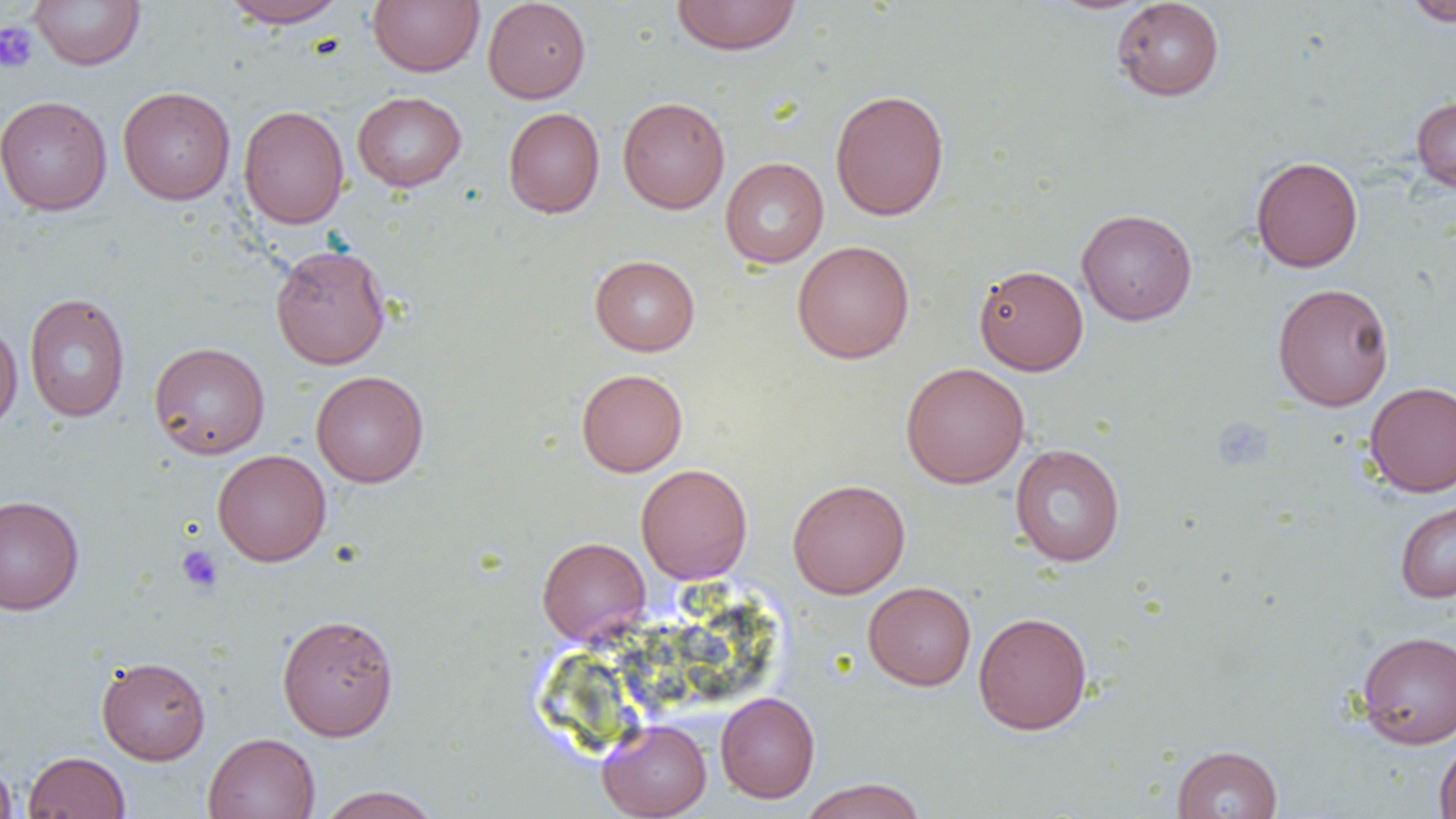

slide-level diagnosis = no evidence of blood parasites
uninfected red blood cell locations = approximate bounding boxes as named x1/y1/x2/y2 corners in pixels: (x1=29, y1=0, x2=145, y2=70), (x1=219, y1=0, x2=350, y2=28), (x1=367, y1=0, x2=484, y2=76), (x1=482, y1=0, x2=591, y2=103), (x1=670, y1=0, x2=801, y2=55), (x1=1112, y1=0, x2=1225, y2=101), (x1=1404, y1=0, x2=1456, y2=25), (x1=118, y1=86, x2=235, y2=205), (x1=830, y1=88, x2=950, y2=221), (x1=352, y1=91, x2=466, y2=192), (x1=0, y1=95, x2=112, y2=216), (x1=618, y1=96, x2=730, y2=213), (x1=1411, y1=97, x2=1456, y2=194), (x1=238, y1=105, x2=349, y2=229), (x1=503, y1=107, x2=604, y2=218), (x1=1251, y1=156, x2=1363, y2=272), (x1=720, y1=157, x2=829, y2=268), (x1=1076, y1=208, x2=1197, y2=325), (x1=792, y1=240, x2=914, y2=363), (x1=271, y1=243, x2=391, y2=369), (x1=589, y1=254, x2=700, y2=356), (x1=974, y1=264, x2=1088, y2=375), (x1=1272, y1=282, x2=1394, y2=412), (x1=24, y1=293, x2=130, y2=422), (x1=0, y1=317, x2=23, y2=434), (x1=148, y1=341, x2=270, y2=459), (x1=901, y1=362, x2=1030, y2=489), (x1=576, y1=368, x2=688, y2=476), (x1=310, y1=370, x2=429, y2=487), (x1=1364, y1=381, x2=1456, y2=497), (x1=1009, y1=444, x2=1125, y2=567), (x1=212, y1=449, x2=331, y2=567), (x1=636, y1=463, x2=753, y2=584), (x1=787, y1=478, x2=910, y2=598), (x1=0, y1=495, x2=84, y2=615), (x1=1395, y1=499, x2=1456, y2=603), (x1=536, y1=536, x2=651, y2=646), (x1=863, y1=582, x2=976, y2=690), (x1=973, y1=611, x2=1092, y2=735), (x1=276, y1=613, x2=399, y2=741), (x1=1356, y1=631, x2=1456, y2=748), (x1=97, y1=656, x2=210, y2=764), (x1=716, y1=692, x2=820, y2=803), (x1=598, y1=718, x2=712, y2=818), (x1=203, y1=732, x2=320, y2=819), (x1=1434, y1=738, x2=1456, y2=819), (x1=1171, y1=745, x2=1283, y2=819), (x1=23, y1=751, x2=130, y2=819), (x1=0, y1=758, x2=18, y2=818), (x1=798, y1=778, x2=928, y2=819), (x1=316, y1=785, x2=443, y2=819)
magnification = 1000x
field of view = single
platelet locations = approximate bounding boxes as named x1/y1/x2/y2 corners in pixels: (x1=0, y1=21, x2=38, y2=74), (x1=1212, y1=417, x2=1274, y2=471), (x1=176, y1=545, x2=224, y2=594)
preparation = thin blood film
modality = light microscopy
image size = 1456×819 pixels